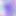
400x magnification. Toxoplasma gondii is seen. Photomicrograph.